Locate every blood parasite and identify its species.
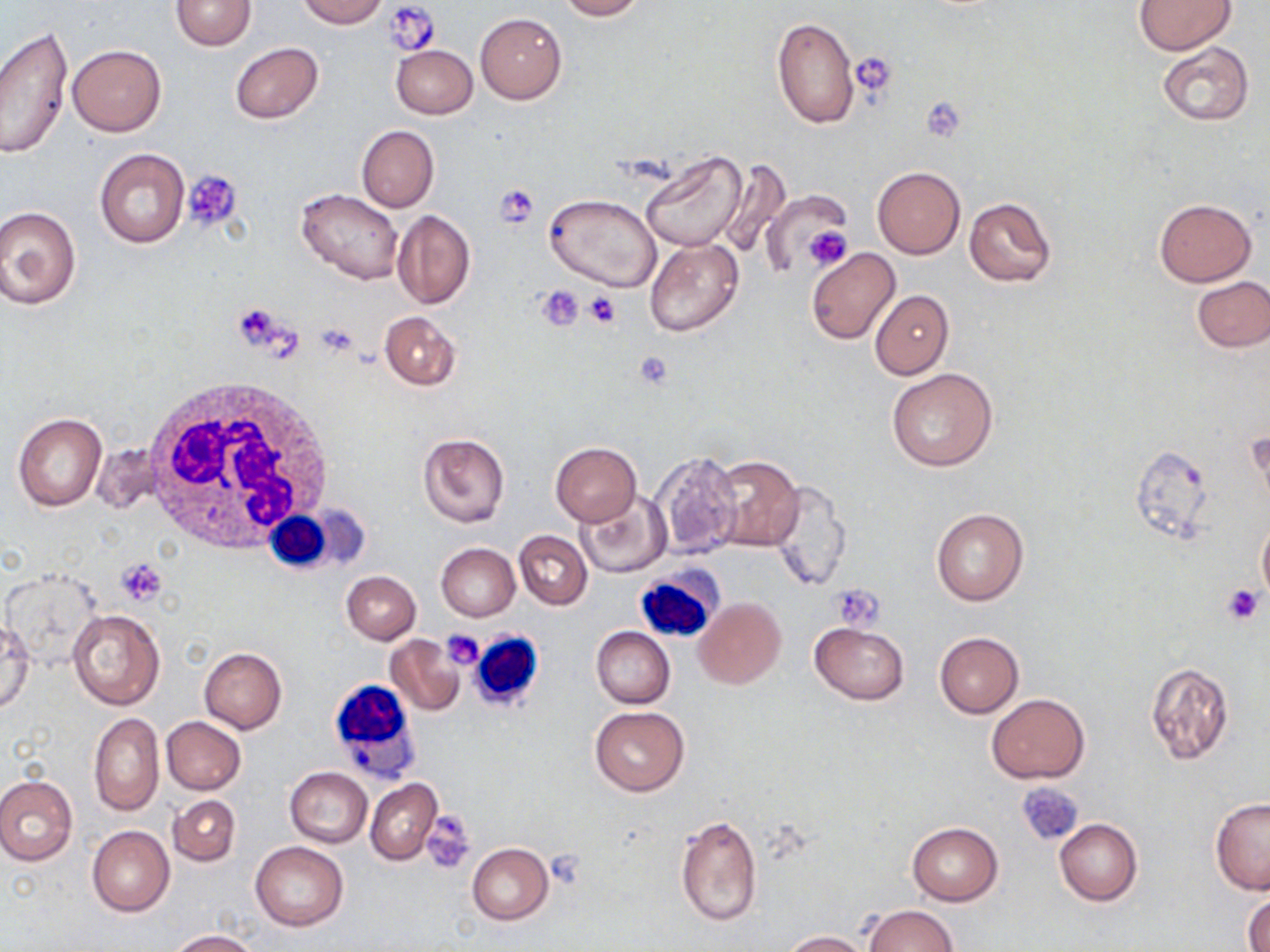
No blood parasites observed.

Summary:
  - Coordinate format: approximate bounding boxes as named x1/y1/x2/y2 corners in pixels
  - Platelet locations: (x1=384, y1=0, x2=439, y2=58), (x1=850, y1=50, x2=898, y2=99), (x1=922, y1=97, x2=966, y2=141), (x1=182, y1=170, x2=243, y2=233), (x1=493, y1=184, x2=540, y2=228), (x1=803, y1=225, x2=852, y2=271), (x1=539, y1=286, x2=583, y2=330), (x1=584, y1=292, x2=621, y2=329), (x1=232, y1=301, x2=290, y2=355), (x1=315, y1=320, x2=360, y2=357), (x1=634, y1=350, x2=676, y2=389), (x1=116, y1=557, x2=169, y2=605), (x1=830, y1=584, x2=884, y2=628), (x1=1221, y1=584, x2=1266, y2=626), (x1=441, y1=631, x2=484, y2=670), (x1=422, y1=809, x2=476, y2=874), (x1=544, y1=850, x2=588, y2=889)
  - White blood cell locations: (x1=138, y1=380, x2=337, y2=551), (x1=263, y1=508, x2=352, y2=574), (x1=635, y1=566, x2=723, y2=645), (x1=469, y1=631, x2=546, y2=712), (x1=329, y1=683, x2=427, y2=806)
  - Uninfected red blood cell locations: (x1=170, y1=0, x2=255, y2=50), (x1=296, y1=0, x2=387, y2=28), (x1=555, y1=0, x2=644, y2=20), (x1=1135, y1=1, x2=1234, y2=54), (x1=475, y1=12, x2=566, y2=104), (x1=772, y1=17, x2=859, y2=131), (x1=0, y1=26, x2=73, y2=158), (x1=231, y1=42, x2=323, y2=123), (x1=1157, y1=43, x2=1254, y2=125), (x1=390, y1=44, x2=477, y2=119), (x1=68, y1=45, x2=166, y2=136), (x1=357, y1=126, x2=439, y2=212), (x1=94, y1=148, x2=190, y2=248), (x1=638, y1=150, x2=747, y2=253), (x1=714, y1=159, x2=791, y2=263), (x1=872, y1=166, x2=965, y2=258), (x1=297, y1=187, x2=403, y2=284), (x1=546, y1=193, x2=661, y2=293), (x1=964, y1=196, x2=1056, y2=288), (x1=1154, y1=198, x2=1257, y2=286), (x1=1, y1=206, x2=82, y2=309), (x1=392, y1=210, x2=475, y2=309), (x1=645, y1=239, x2=742, y2=337), (x1=806, y1=248, x2=901, y2=345), (x1=1191, y1=275, x2=1269, y2=352), (x1=869, y1=290, x2=952, y2=379), (x1=380, y1=311, x2=459, y2=390), (x1=886, y1=368, x2=999, y2=472), (x1=13, y1=413, x2=106, y2=511), (x1=417, y1=431, x2=510, y2=529), (x1=550, y1=441, x2=642, y2=526), (x1=1129, y1=442, x2=1214, y2=541), (x1=651, y1=451, x2=742, y2=558), (x1=705, y1=454, x2=805, y2=553), (x1=770, y1=480, x2=850, y2=592), (x1=577, y1=493, x2=671, y2=578), (x1=931, y1=508, x2=1029, y2=606), (x1=1257, y1=516, x2=1270, y2=602), (x1=514, y1=531, x2=591, y2=608), (x1=436, y1=543, x2=520, y2=621), (x1=341, y1=571, x2=420, y2=644), (x1=694, y1=597, x2=786, y2=689), (x1=68, y1=610, x2=164, y2=710), (x1=0, y1=619, x2=34, y2=715), (x1=810, y1=623, x2=910, y2=704), (x1=591, y1=627, x2=674, y2=709), (x1=934, y1=631, x2=1025, y2=718), (x1=385, y1=634, x2=465, y2=716), (x1=199, y1=648, x2=286, y2=733), (x1=1146, y1=661, x2=1235, y2=765), (x1=986, y1=693, x2=1089, y2=784), (x1=590, y1=706, x2=688, y2=796), (x1=89, y1=712, x2=164, y2=816), (x1=162, y1=717, x2=246, y2=794), (x1=285, y1=767, x2=372, y2=847), (x1=0, y1=775, x2=77, y2=866), (x1=365, y1=779, x2=441, y2=864), (x1=168, y1=795, x2=240, y2=865), (x1=1209, y1=798, x2=1270, y2=895), (x1=674, y1=814, x2=763, y2=928), (x1=1054, y1=818, x2=1143, y2=906), (x1=907, y1=822, x2=1003, y2=906), (x1=87, y1=826, x2=174, y2=916), (x1=250, y1=842, x2=349, y2=930), (x1=467, y1=844, x2=553, y2=925), (x1=1244, y1=891, x2=1270, y2=950), (x1=865, y1=905, x2=960, y2=951), (x1=167, y1=930, x2=260, y2=951), (x1=782, y1=930, x2=873, y2=952)
  - Slide-level diagnosis: negative for blood parasites
  - Modality: optical microscopy
  - Image size: 1270×952 pixels
  - Preparation: thin blood smear
  - Field of view: one of a larger specimen
  - Stain: May-Grünwald-Giemsa
  - Magnification: 1000x